Classify this cell by malaria status.
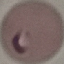
It is parasitized.

capture = smartphone through the microscope eyepiece
stain = Giemsa
image type = automatically extracted cell patch, resized to 64 × 64 pixels
preparation = thin blood smear